Report the malaria status of this cell.
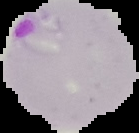

Parasitized.

Summary:
  - Image type: segmented cell region with the area outside set to black
  - Image size: 139×133 pixels
  - Preparation: thin blood smear